Report the malaria status of this cell.
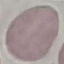
Uninfected.

image type = automatically extracted cell patch, resized to 64 × 64 pixels
stain = Giemsa
preparation = thin blood film
capture = smartphone camera at the microscope eyepiece